Give the position of every leukocyte.
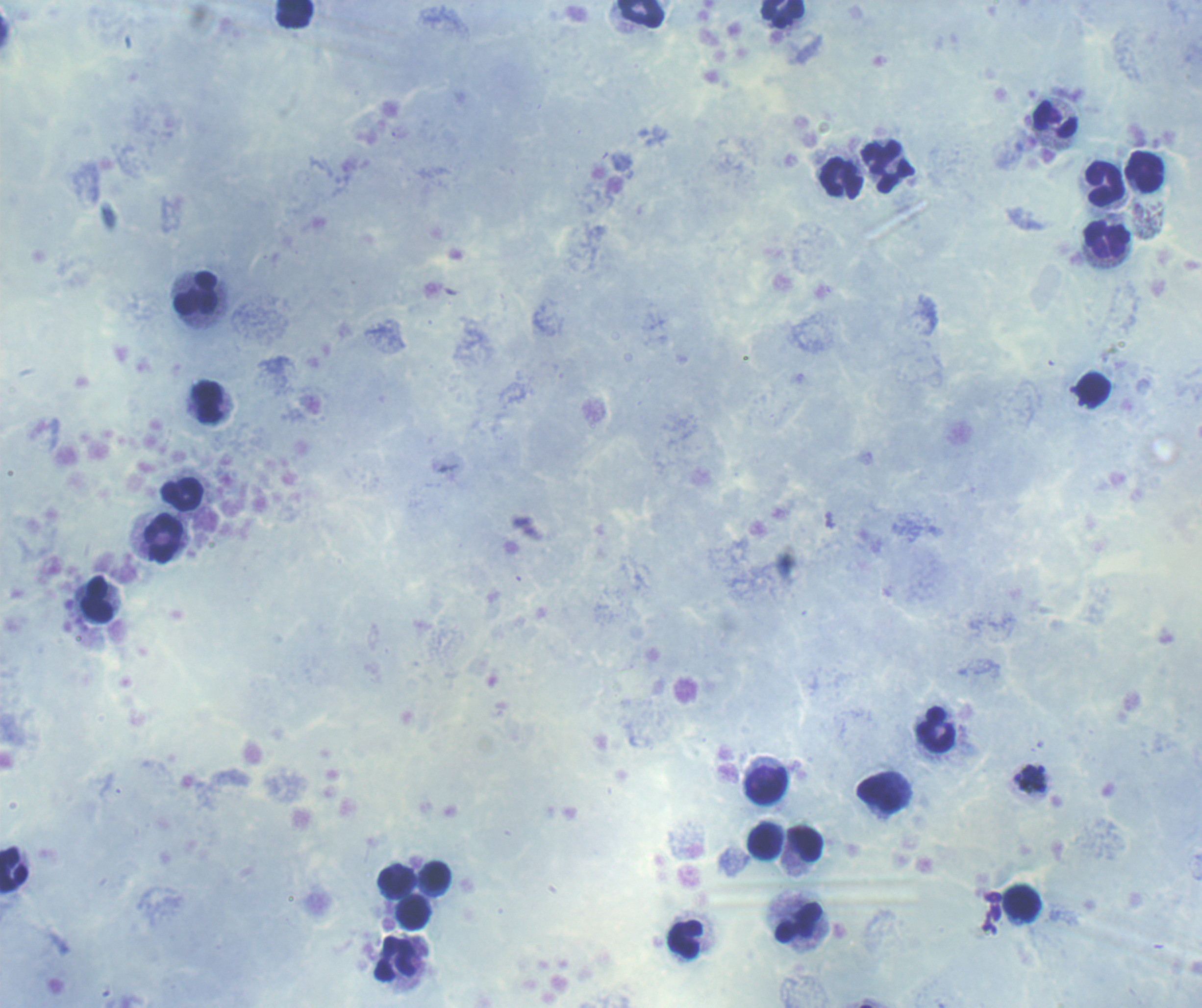

Approximate centers as (x, y) in pixels.
Leukocytes: (639, 13), (294, 14), (783, 14), (1055, 120), (888, 168), (1145, 172), (842, 178), (1104, 184), (1106, 239), (196, 295), (207, 402), (182, 495), (164, 538), (97, 599), (937, 729), (766, 785), (880, 794), (764, 842), (805, 844), (13, 869), (434, 876), (396, 882), (1022, 903), (413, 912), (798, 922), (685, 939), (395, 958).

Approximate centers as (x, y) in pixels. Schizont locations: (1030, 779). Coloration quality: good. Background quality: satisfactory. Result: Plasmodium parasites identified. Romanowsky stain. Thick blood film. Previously used in an actual diagnosis. 100x magnification. Image is 1202×1008 pixels. One field from this slide.